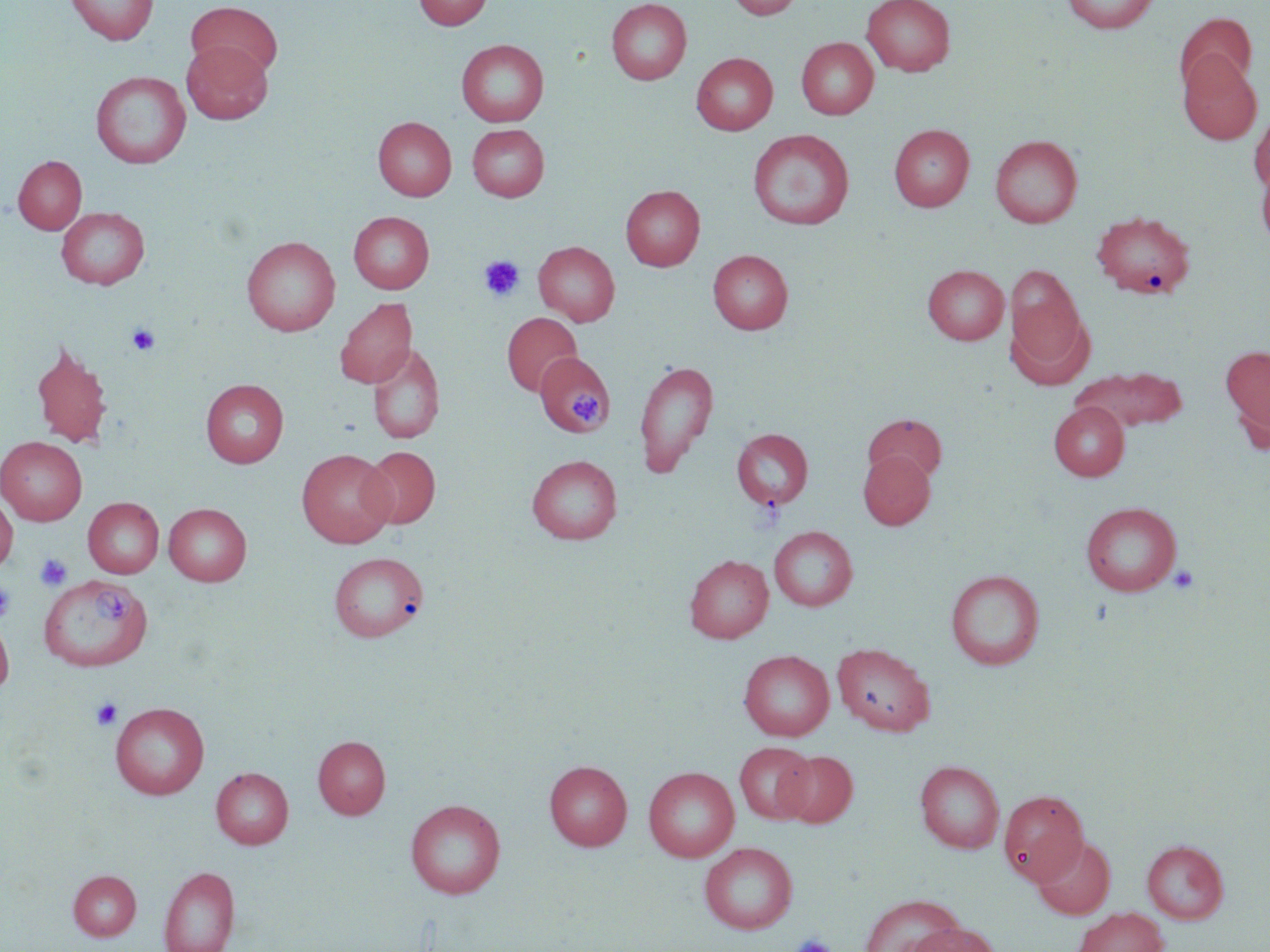

Approximate bounding boxes as [x1, y1, x2, y2] in pixels. Uninfected red blood cell locations: [66, 0, 158, 45], [413, 0, 492, 31], [606, 0, 692, 85], [727, 0, 803, 19], [862, 0, 955, 76], [1061, 0, 1159, 34], [186, 2, 283, 81], [1174, 12, 1256, 99], [797, 37, 878, 120], [456, 39, 548, 127], [182, 40, 272, 124], [691, 52, 778, 135], [1178, 52, 1262, 145], [90, 71, 191, 169], [1249, 108, 1270, 195], [374, 117, 456, 201], [467, 124, 549, 201], [889, 124, 974, 212], [748, 129, 854, 230], [990, 135, 1082, 228], [13, 155, 87, 235], [1256, 156, 1270, 251], [621, 185, 705, 271], [56, 206, 150, 289], [1092, 210, 1196, 299], [348, 211, 434, 293], [242, 236, 340, 336], [534, 241, 620, 326], [708, 250, 793, 334], [922, 264, 1010, 344], [1005, 265, 1086, 369], [334, 297, 417, 389], [502, 312, 582, 396], [30, 340, 114, 451], [367, 342, 445, 445], [1221, 345, 1270, 444], [537, 353, 613, 436], [634, 359, 719, 476], [1079, 367, 1188, 431], [201, 379, 288, 468], [1049, 401, 1129, 481], [863, 413, 948, 484], [732, 428, 814, 510], [0, 436, 87, 525], [360, 446, 440, 529], [296, 449, 396, 547], [858, 450, 935, 530], [527, 455, 622, 544], [0, 495, 17, 575], [83, 497, 164, 578], [1081, 501, 1182, 596], [164, 503, 251, 586], [769, 526, 858, 611], [329, 552, 428, 642], [685, 554, 774, 643], [945, 569, 1045, 670], [39, 574, 152, 671], [0, 613, 14, 698], [833, 643, 935, 735], [739, 650, 834, 740], [110, 702, 209, 799], [313, 735, 390, 819], [735, 742, 816, 823], [778, 750, 858, 827], [544, 760, 632, 851], [915, 761, 1004, 853], [643, 766, 739, 862], [211, 767, 293, 849], [998, 789, 1089, 885], [405, 799, 505, 898], [1032, 836, 1116, 919], [1141, 840, 1229, 924], [700, 842, 797, 934], [158, 866, 240, 952], [68, 870, 141, 940], [860, 894, 965, 952], [1073, 907, 1169, 952], [905, 920, 1001, 952]. Platelet locations: [479, 255, 525, 301], [126, 323, 161, 356], [569, 390, 601, 428], [35, 553, 72, 591], [1167, 564, 1200, 596], [0, 582, 14, 622], [90, 590, 136, 627], [91, 698, 122, 730], [790, 934, 835, 952]. Slide-level diagnosis: negative for blood parasites. Image is 1270×952 pixels. Thin blood film. Light microscopy. Captured at 1000x magnification. One field of a larger specimen. May-Grünwald-Giemsa-stained preparation.